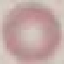 Malaria status: uninfected. Thin smear of blood. Giemsa-stained preparation. Automatically extracted cell patch, resized to 64 × 64 pixels. Acquired by smartphone through the microscope eyepiece.